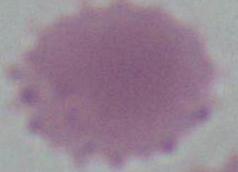
Summary:
  - Magnification: 1000x
  - Modality: micrograph
  - Identification: erythrocyte